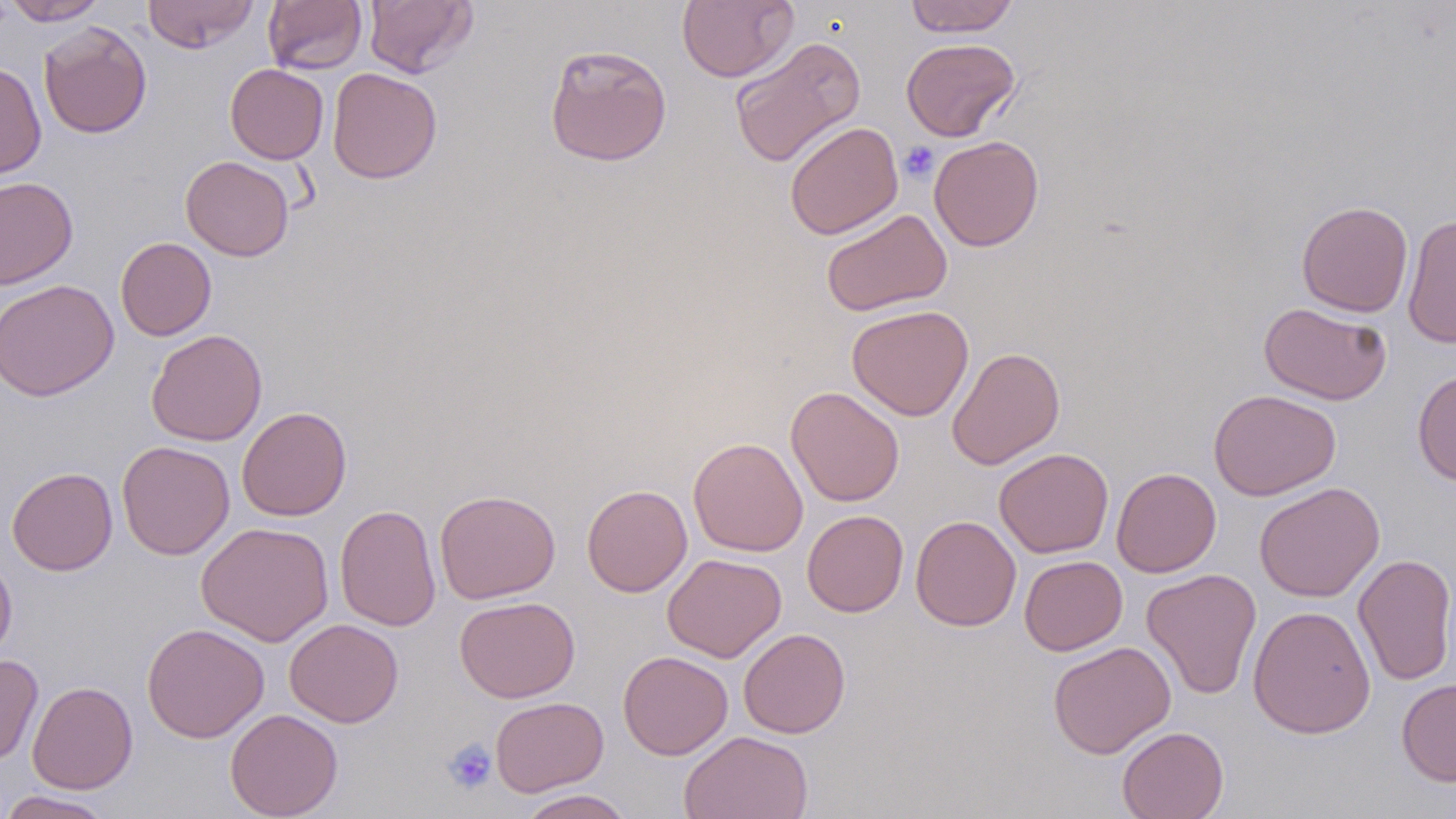
slide-level diagnosis = negative for blood parasites
modality = light microscopy
magnification = 1000x
field of view = one of a larger specimen
image size = 1456×819 pixels
uninfected red blood cell locations = approximate bounding boxes as [x1, y1, x2, y2] in pixels: [2, 0, 109, 26], [141, 0, 260, 52], [363, 0, 478, 77], [677, 0, 798, 82], [904, 0, 1020, 37], [263, 1, 368, 75], [38, 21, 152, 139], [728, 36, 866, 167], [901, 37, 1021, 142], [544, 43, 672, 167], [0, 61, 47, 180], [225, 63, 329, 164], [327, 67, 442, 184], [784, 121, 903, 240], [929, 135, 1044, 251], [180, 156, 295, 262], [0, 176, 78, 289], [1297, 200, 1413, 317], [820, 208, 952, 316], [1402, 214, 1456, 349], [115, 237, 217, 340], [0, 279, 118, 401], [1259, 301, 1392, 405], [846, 304, 974, 421], [146, 329, 268, 446], [947, 346, 1065, 470], [1412, 369, 1456, 486], [786, 386, 904, 507], [1209, 389, 1341, 500], [237, 406, 352, 521], [688, 437, 809, 557], [116, 441, 235, 560], [994, 448, 1114, 558], [7, 467, 118, 576], [1111, 467, 1221, 577], [1254, 481, 1384, 603], [581, 484, 692, 597], [434, 488, 561, 604], [334, 503, 441, 632], [802, 509, 908, 617], [910, 515, 1021, 631], [195, 521, 334, 645], [0, 552, 17, 663], [662, 553, 786, 662], [1353, 553, 1456, 687], [1019, 555, 1127, 655], [1142, 568, 1262, 700], [454, 596, 580, 702], [1248, 605, 1376, 739], [284, 618, 404, 728], [142, 623, 269, 743], [738, 628, 850, 738], [1048, 641, 1175, 759], [618, 650, 733, 760], [0, 655, 44, 765], [1396, 677, 1456, 786], [27, 680, 138, 794], [490, 696, 609, 796], [225, 708, 343, 818], [1116, 726, 1229, 819], [679, 730, 813, 818], [515, 789, 636, 818], [0, 790, 117, 819]
stain = May-Grünwald-Giemsa
preparation = thin blood smear
platelet locations = approximate bounding boxes as [x1, y1, x2, y2] in pixels: [899, 142, 939, 182], [444, 739, 497, 793]